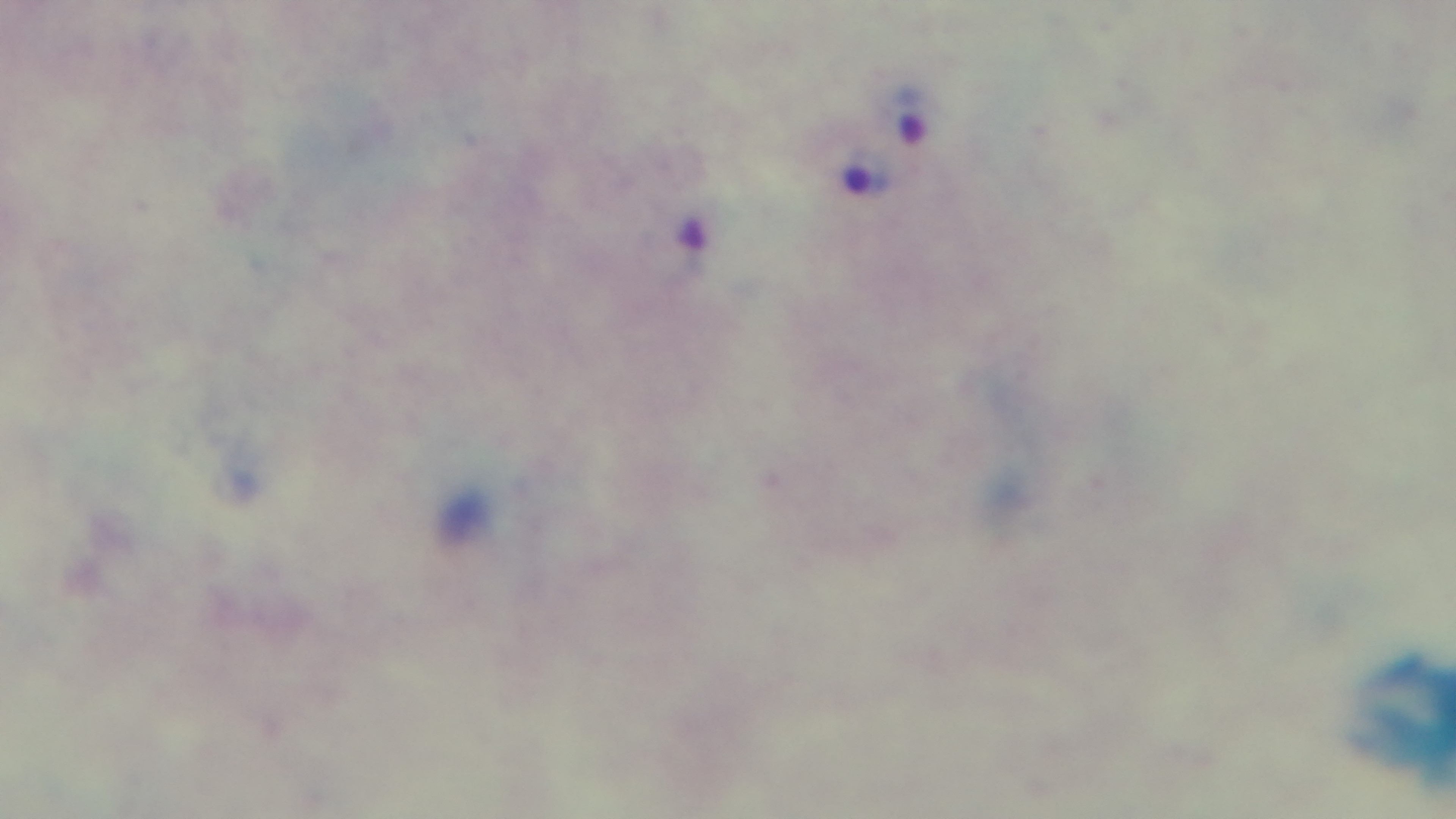
Malaria status: positive. Mounted 4K digital camera. Photomicrograph. Preparation: thick blood film. Giemsa stain. One field from the slide. Oil-immersion objective, 100x.